Assess this cell for malaria.
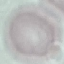

Uninfected.

Giemsa stain. Automatically extracted cell patch, resized to 64 × 64 pixels. Acquired by smartphone through the microscope eyepiece. Thin blood smear.